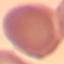

Summary:
  - Result: negative for malaria parasites
  - Capture: smartphone through the microscope eyepiece
  - Stain: Giemsa
  - Preparation: thin smear
  - Image type: cell patch, automatically extracted from a larger field of view and resized to 64 × 64 pixels